State which parasite is depicted.
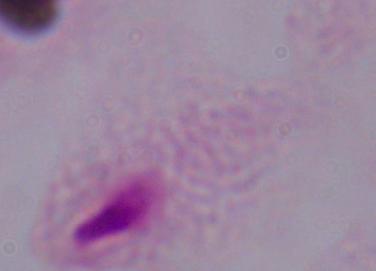
This is a trichomonad.

1000x magnification. Micrograph.